Locate every blood parasite and identify its species.
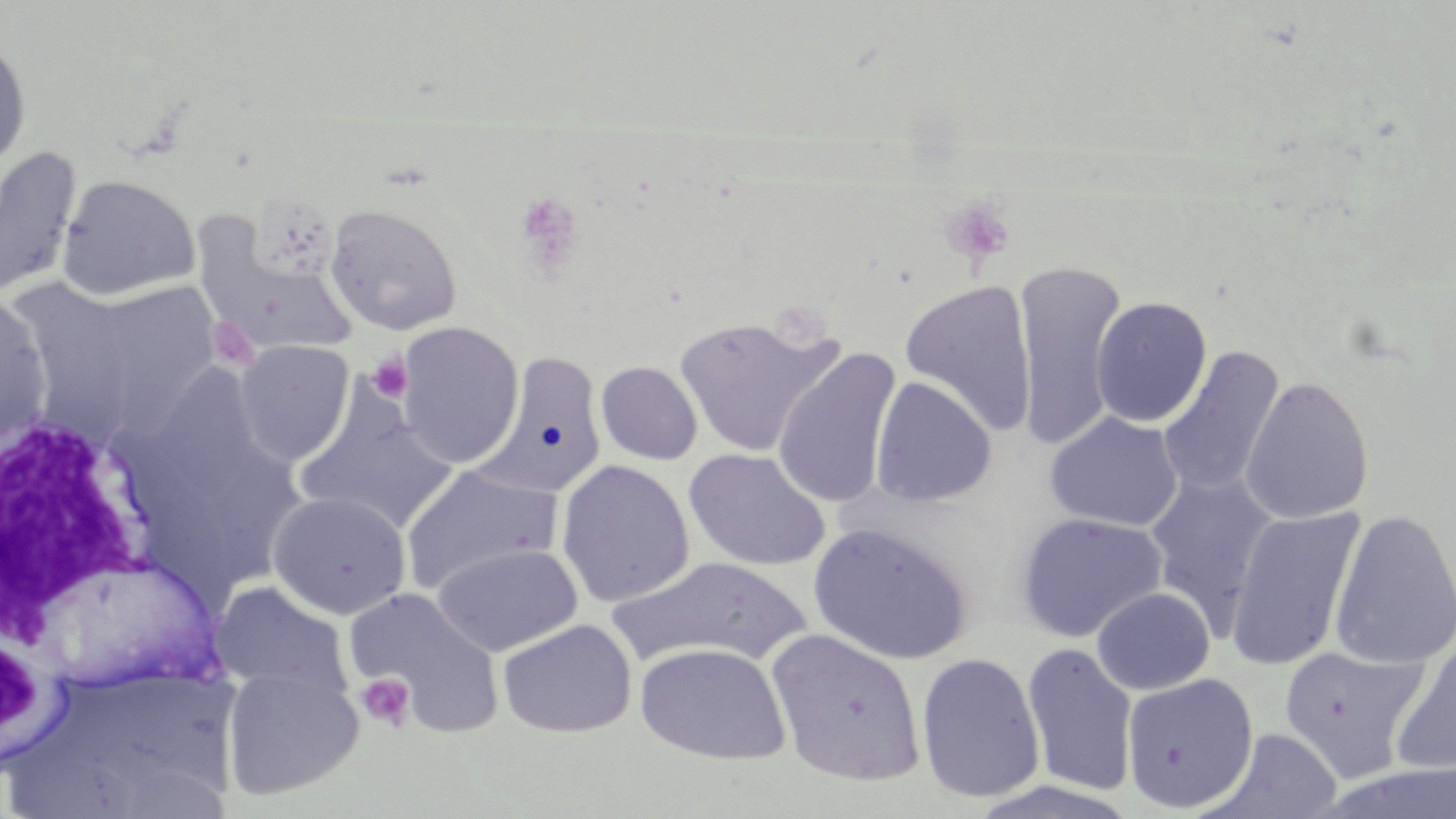
No blood parasites observed.

Approximate bounding boxes as [x1, y1, x2, y2] in pixels. Uninfected red blood cell locations: [0, 36, 33, 177], [0, 147, 81, 301], [58, 174, 200, 301], [325, 203, 462, 336], [209, 255, 359, 358], [1014, 261, 1128, 451], [69, 280, 221, 435], [898, 280, 1038, 437], [0, 290, 53, 451], [1090, 296, 1212, 427], [672, 315, 841, 457], [395, 321, 524, 468], [233, 340, 354, 465], [1158, 345, 1285, 500], [772, 346, 902, 511], [481, 354, 608, 502], [595, 361, 703, 465], [1239, 375, 1375, 525], [870, 377, 997, 507], [294, 392, 458, 535], [1043, 412, 1184, 531], [683, 448, 831, 572], [555, 459, 695, 607], [400, 463, 561, 596], [1145, 471, 1278, 629], [267, 491, 412, 620], [1224, 506, 1365, 671], [1329, 508, 1456, 669], [1015, 512, 1167, 643], [808, 523, 973, 666], [430, 542, 584, 657], [29, 555, 223, 692], [606, 556, 810, 669], [209, 581, 354, 703], [1091, 586, 1215, 694], [344, 587, 504, 736], [496, 618, 637, 737], [766, 628, 927, 786], [1389, 636, 1456, 775], [634, 642, 791, 765], [1021, 643, 1139, 797], [1278, 645, 1430, 783], [915, 651, 1046, 803], [220, 663, 364, 801], [1121, 671, 1259, 814], [1216, 728, 1342, 818]. Platelet locations: [515, 190, 585, 275], [938, 195, 1014, 267], [207, 316, 261, 372], [367, 352, 414, 403], [356, 672, 416, 732]. White blood cell locations: [1, 409, 160, 638]. Slide-level diagnosis: no evidence of blood parasites. Thin blood film. May-Grünwald-Giemsa stain. Single field of view. 1000x magnification. Light microscopy. Image is 1456×819 pixels.